Report the malaria status of this cell.
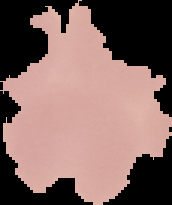

Parasitized.

{
  "preparation": "thin blood film",
  "image_size": "172×205 pixels",
  "image_type": "cell region segmented out of the field of view; surrounding area masked to black"
}